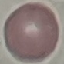
result = negative for malaria parasites
stain = Giemsa
preparation = thin smear
capture = smartphone through the microscope eyepiece
image type = cell patch, automatically extracted from a larger field of view and resized to 64 × 64 pixels